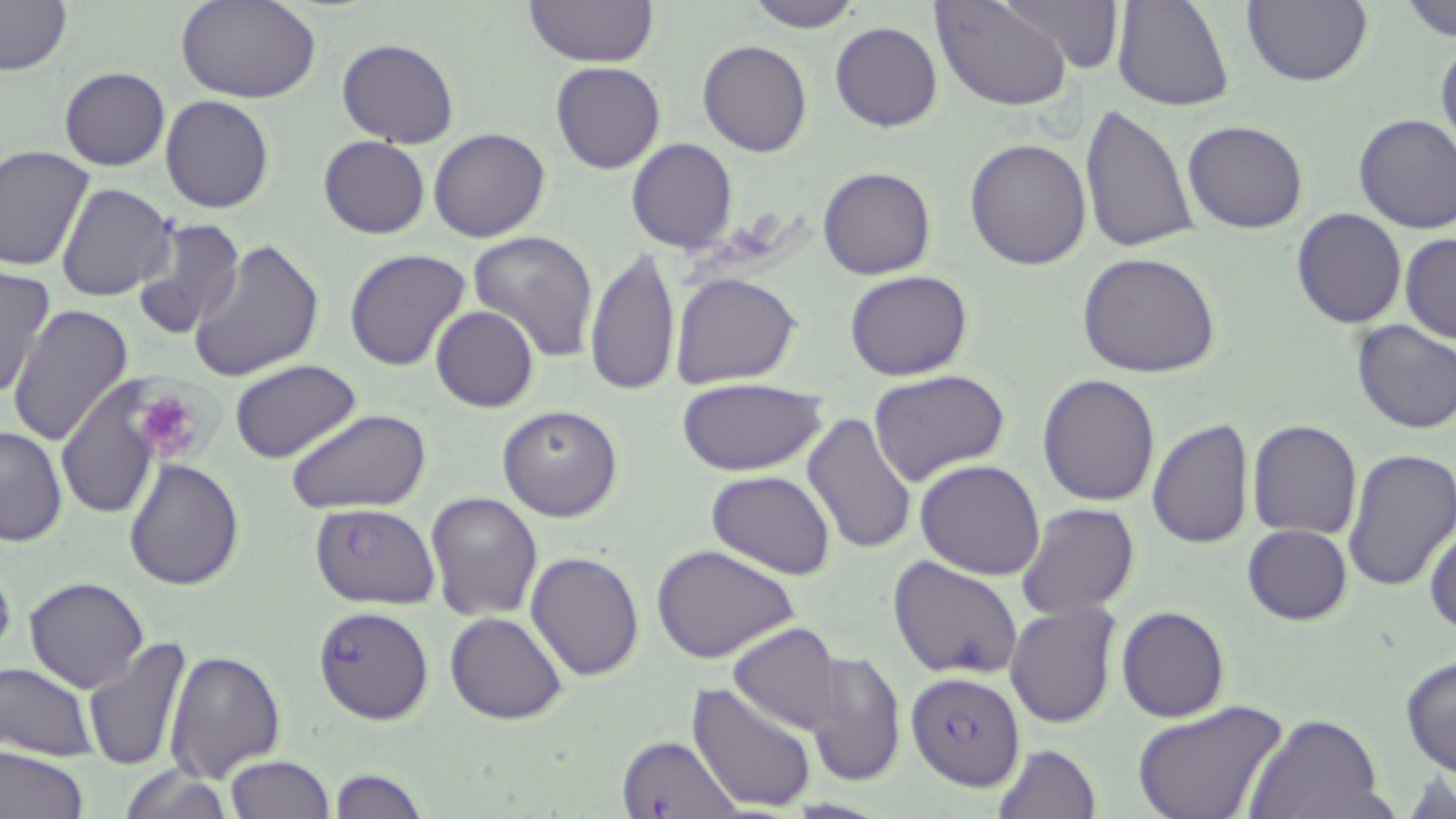 Approximate bounding boxes as named x1/y1/x2/y2 corners in pixels. Plasmodium falciparum-infected red blood cell locations: (x1=309, y1=503, x2=441, y2=609), (x1=312, y1=605, x2=434, y2=725), (x1=907, y1=671, x2=1025, y2=790), (x1=616, y1=733, x2=741, y2=818). Platelet locations: (x1=130, y1=385, x2=211, y2=464). Uninfected red blood cell locations: (x1=0, y1=0, x2=73, y2=76), (x1=177, y1=0, x2=320, y2=104), (x1=523, y1=0, x2=660, y2=68), (x1=743, y1=0, x2=868, y2=32), (x1=931, y1=0, x2=1072, y2=111), (x1=998, y1=0, x2=1125, y2=73), (x1=1111, y1=0, x2=1235, y2=113), (x1=1242, y1=0, x2=1370, y2=88), (x1=1401, y1=0, x2=1456, y2=39), (x1=830, y1=22, x2=942, y2=132), (x1=1435, y1=37, x2=1456, y2=159), (x1=336, y1=39, x2=459, y2=149), (x1=697, y1=39, x2=812, y2=157), (x1=550, y1=61, x2=665, y2=174), (x1=59, y1=66, x2=170, y2=171), (x1=159, y1=94, x2=276, y2=213), (x1=1079, y1=102, x2=1199, y2=255), (x1=1353, y1=113, x2=1456, y2=234), (x1=1183, y1=120, x2=1309, y2=234), (x1=428, y1=129, x2=550, y2=242), (x1=317, y1=136, x2=430, y2=239), (x1=627, y1=138, x2=738, y2=255), (x1=965, y1=138, x2=1092, y2=269), (x1=0, y1=146, x2=95, y2=270), (x1=818, y1=167, x2=936, y2=280), (x1=56, y1=183, x2=177, y2=301), (x1=1293, y1=208, x2=1406, y2=327), (x1=131, y1=215, x2=247, y2=340), (x1=467, y1=230, x2=599, y2=361), (x1=1400, y1=232, x2=1456, y2=343), (x1=186, y1=238, x2=325, y2=383), (x1=583, y1=248, x2=683, y2=397), (x1=343, y1=249, x2=472, y2=372), (x1=1077, y1=251, x2=1222, y2=378), (x1=0, y1=265, x2=54, y2=401), (x1=844, y1=270, x2=973, y2=381), (x1=670, y1=271, x2=802, y2=388), (x1=6, y1=305, x2=135, y2=444), (x1=431, y1=306, x2=539, y2=412), (x1=1351, y1=319, x2=1456, y2=434), (x1=231, y1=360, x2=363, y2=464), (x1=867, y1=370, x2=1010, y2=490), (x1=1037, y1=374, x2=1160, y2=506), (x1=677, y1=378, x2=827, y2=476), (x1=58, y1=381, x2=160, y2=518), (x1=497, y1=405, x2=623, y2=522), (x1=287, y1=407, x2=433, y2=516), (x1=802, y1=412, x2=917, y2=554), (x1=1148, y1=418, x2=1254, y2=550), (x1=1248, y1=419, x2=1361, y2=538), (x1=0, y1=425, x2=67, y2=548), (x1=1343, y1=448, x2=1456, y2=592), (x1=123, y1=457, x2=244, y2=592), (x1=915, y1=460, x2=1045, y2=580), (x1=706, y1=469, x2=837, y2=579), (x1=423, y1=491, x2=543, y2=621), (x1=1015, y1=502, x2=1142, y2=622), (x1=1426, y1=517, x2=1456, y2=637), (x1=1242, y1=525, x2=1351, y2=626), (x1=652, y1=544, x2=801, y2=664), (x1=526, y1=551, x2=644, y2=683), (x1=887, y1=553, x2=1023, y2=680), (x1=0, y1=558, x2=18, y2=674), (x1=25, y1=576, x2=147, y2=692), (x1=1005, y1=601, x2=1121, y2=729), (x1=1116, y1=605, x2=1229, y2=722), (x1=445, y1=612, x2=568, y2=725), (x1=727, y1=623, x2=843, y2=736), (x1=81, y1=636, x2=194, y2=772), (x1=164, y1=647, x2=286, y2=782), (x1=805, y1=651, x2=905, y2=788), (x1=1399, y1=655, x2=1456, y2=777), (x1=1, y1=662, x2=101, y2=761), (x1=686, y1=682, x2=819, y2=813), (x1=1131, y1=700, x2=1287, y2=819), (x1=1246, y1=714, x2=1386, y2=819), (x1=993, y1=741, x2=1101, y2=818), (x1=0, y1=744, x2=89, y2=819), (x1=224, y1=756, x2=333, y2=818), (x1=115, y1=765, x2=235, y2=818), (x1=328, y1=766, x2=426, y2=819). Slide-level diagnosis: Plasmodium falciparum. Single field of view. Optical microscopy. Image is 1456×819 pixels. 1000x magnification. Thin blood film. May-Grünwald-Giemsa-stained preparation.